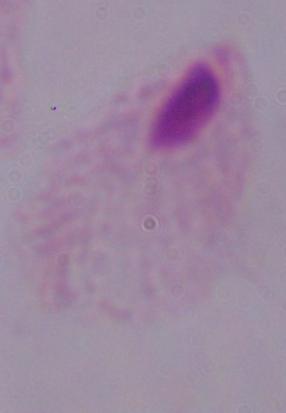

Summary:
  - Identification: trichomonad
  - Magnification: 1000x
  - Modality: micrograph